Classify this cell by malaria status.
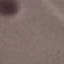
It is uninfected.

Summary:
  - Capture: smartphone camera at the microscope eyepiece
  - Image type: cell patch, automatically extracted from a larger field of view and resized to 64 × 64 pixels
  - Stain: Giemsa
  - Preparation: thin blood film